Give the position of every Plasmodium parasite.
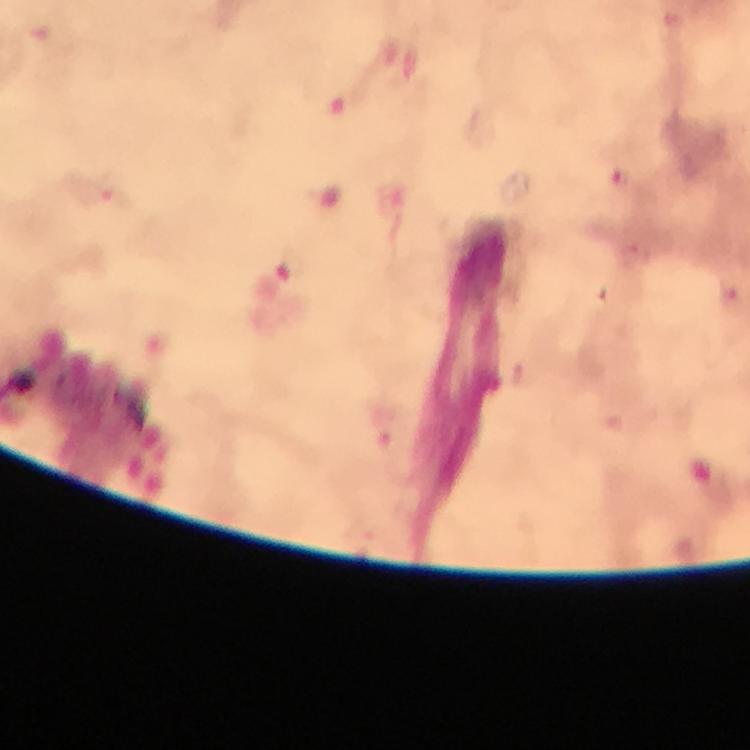

Approximate centers as [x, y] in pixels.
Plasmodium parasites: [621, 175], [107, 188], [290, 266], [733, 297].

immersion_oil: used
stain: Giemsa
cropped_from: a single field of view
context: from a diagnostic examination for malaria
preparation: thick smear
capture: smartphone camera through the microscope
image_size: 750×750 pixels
magnification: 100x